Evaluate for parasitized red blood cells.
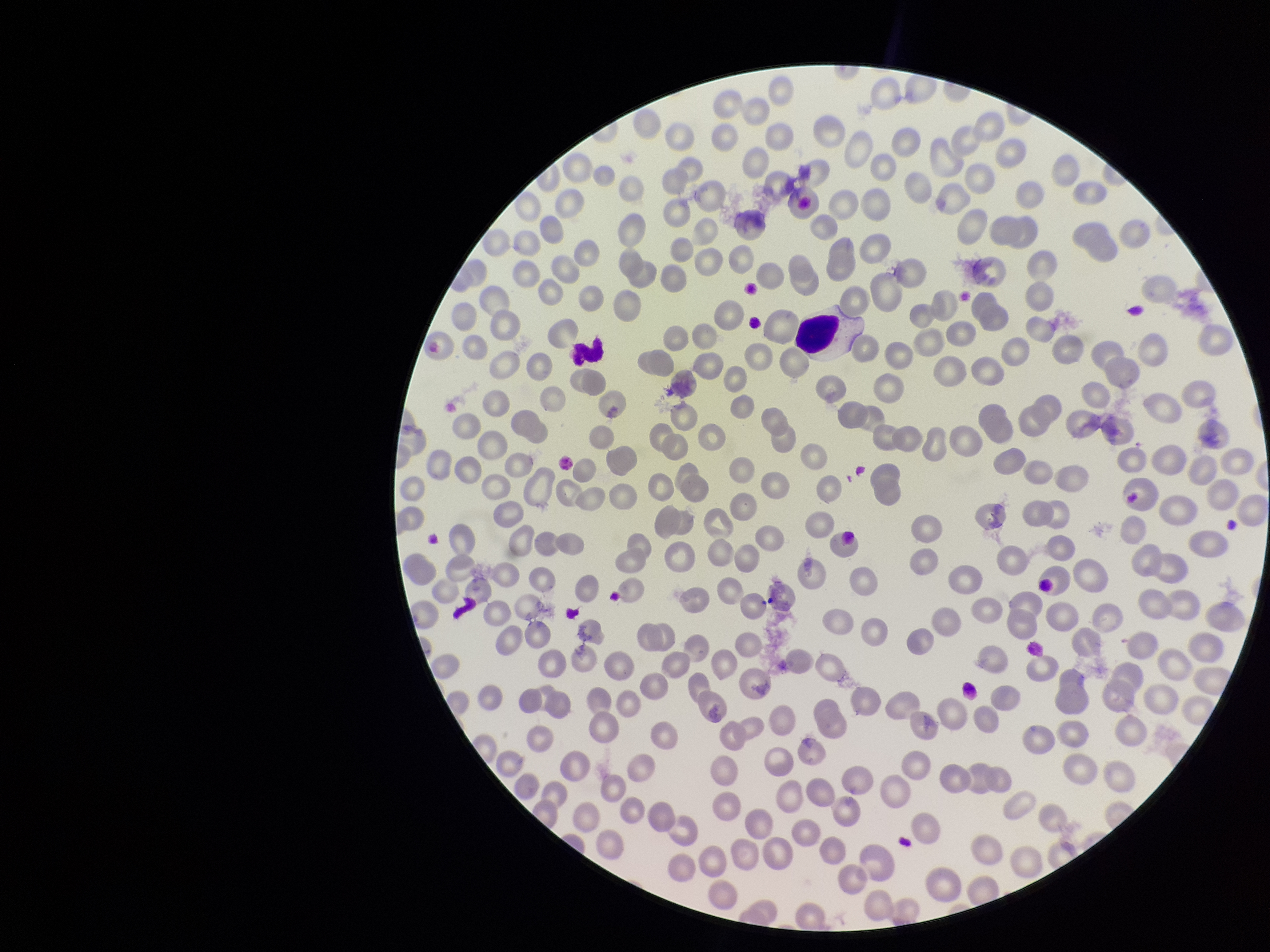

None detected.

Species reported for this patient: Plasmodium falciparum. Image is 1270×952 pixels. One field from this slide. Stained with Giemsa. Red blood cell count: 286. Smartphone photograph taken through the eyepiece of a microscope. Parasitized red blood cell count: 0. Preparation: thin smear. Patient malaria status: positive.